Classify this cell by malaria status.
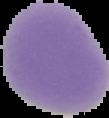
Uninfected.

Summary:
  - Image type: segmented cell region with the area outside set to black
  - Preparation: thin blood smear
  - Image size: 109×118 pixels